Classify this cell by malaria status.
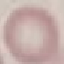
It is uninfected.

stain = Giemsa
capture = smartphone through the microscope eyepiece
preparation = thin smear
image type = cell patch, automatically extracted from a larger field of view and resized to 64 × 64 pixels